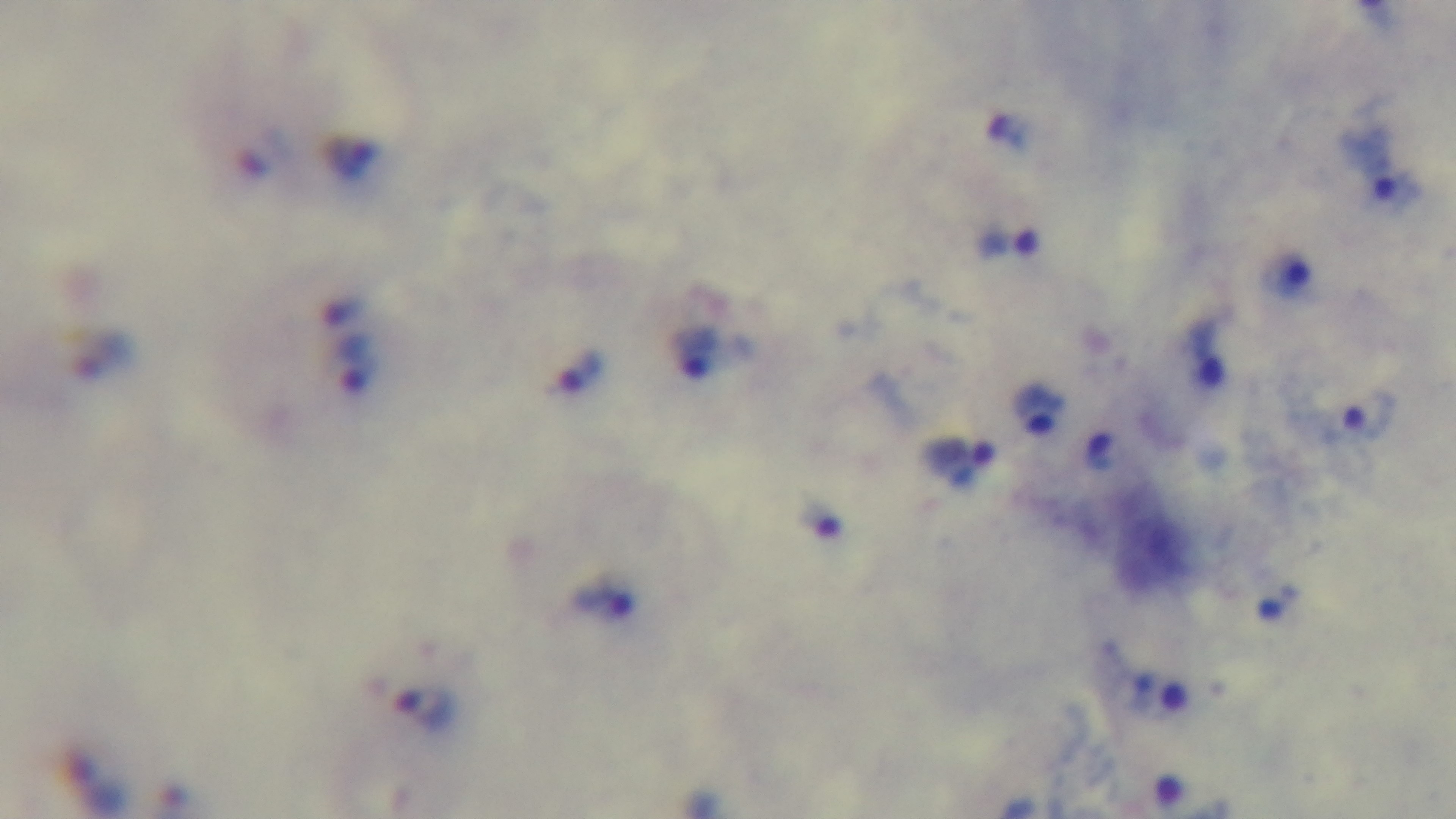 Giemsa stain. Malaria status: infected. 100x oil-immersion objective. Preparation: thick smear. Captured with a mounted 4K digital camera. Light microscopy. Single field of view.